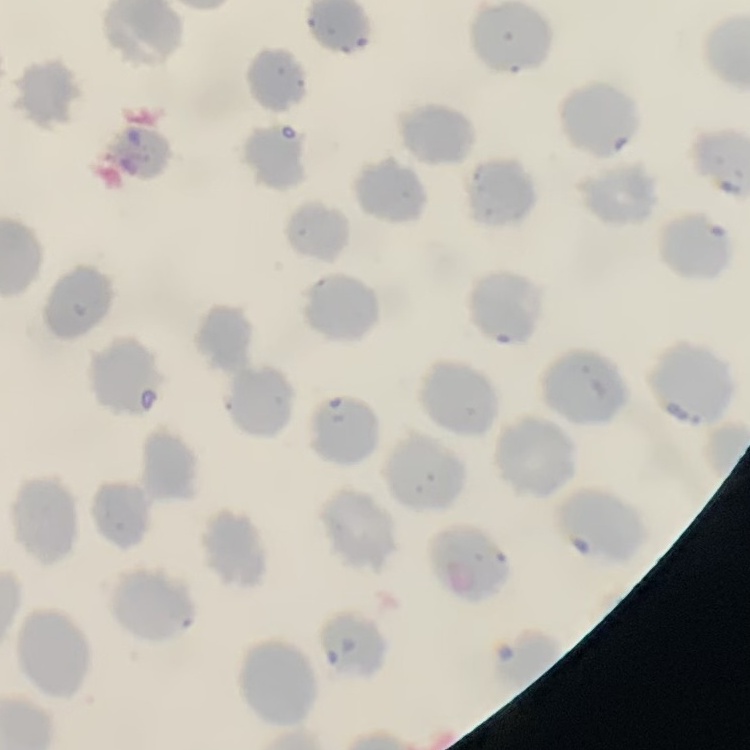
Summary:
  - Erythrocyte morphology: no rouleaux formation
  - Image type: square crop of a larger photomicrograph
  - Stain: Field's or Giemsa
  - Preparation: thin blood film